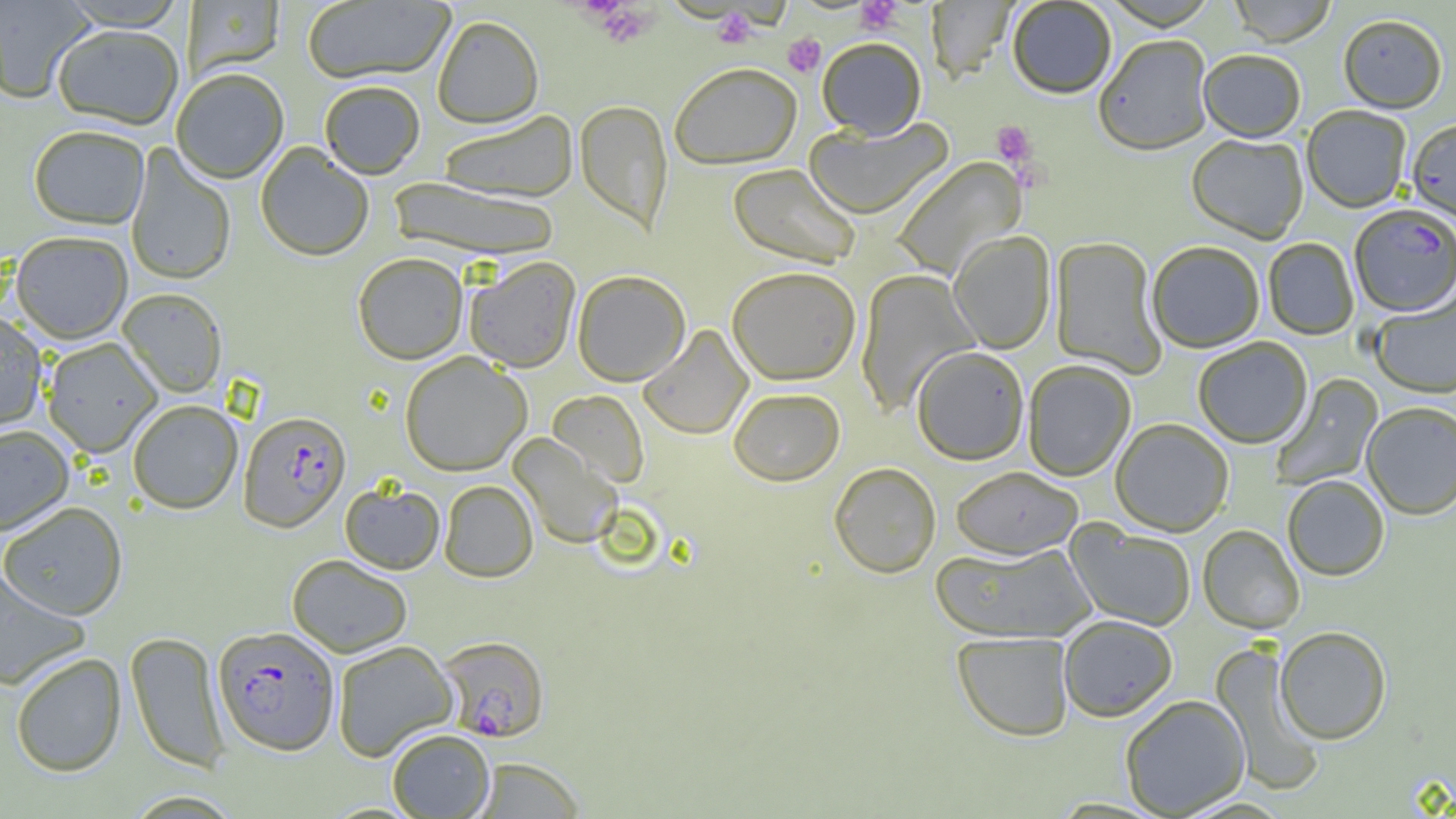

Summary:
  - Coordinate format: approximate bounding boxes as [x1, y1, x2, y2] in pixels
  - Uninfected red blood cell locations: [0, 0, 94, 105], [302, 0, 455, 86], [1102, 0, 1219, 32], [1228, 0, 1337, 48], [59, 1, 190, 32], [184, 1, 285, 80], [310, 1, 438, 178], [926, 1, 1017, 82], [1007, 1, 1116, 101], [433, 17, 544, 130], [1338, 17, 1447, 115], [53, 27, 183, 130], [1095, 38, 1213, 158], [817, 39, 926, 140], [1198, 52, 1305, 144], [670, 63, 802, 170], [171, 70, 288, 185], [319, 82, 425, 180], [575, 100, 673, 235], [1302, 108, 1411, 214], [437, 111, 579, 204], [804, 117, 954, 220], [1406, 120, 1456, 226], [28, 128, 149, 231], [1186, 136, 1308, 244], [125, 144, 236, 287], [255, 144, 374, 262], [891, 157, 1027, 281], [727, 163, 862, 270], [389, 178, 563, 263], [948, 231, 1056, 354], [11, 233, 132, 345], [1050, 237, 1167, 380], [1263, 238, 1358, 340], [1147, 242, 1265, 353], [353, 253, 468, 364], [464, 257, 581, 372], [727, 266, 861, 385], [855, 270, 981, 417], [572, 271, 691, 386], [117, 289, 227, 399], [1370, 291, 1456, 399], [0, 311, 47, 433], [638, 325, 753, 440], [1193, 338, 1313, 449], [42, 339, 162, 458], [912, 346, 1029, 465], [400, 352, 531, 476], [1023, 360, 1136, 481], [1270, 374, 1383, 491], [728, 387, 845, 486], [547, 390, 649, 488], [128, 401, 243, 515], [1362, 403, 1456, 520], [1111, 419, 1234, 537], [0, 426, 74, 535], [508, 433, 622, 549], [829, 462, 941, 578], [950, 466, 1083, 559], [1283, 476, 1389, 582], [439, 480, 538, 582], [340, 482, 445, 574], [0, 502, 127, 621], [1066, 523, 1196, 631], [1198, 525, 1304, 634], [929, 542, 1097, 644], [287, 554, 412, 657], [0, 569, 90, 689], [1059, 616, 1178, 723], [1276, 627, 1391, 745], [125, 631, 229, 774], [952, 632, 1074, 742], [332, 640, 457, 761], [1209, 641, 1327, 796], [11, 653, 126, 778], [1120, 695, 1250, 817], [387, 729, 495, 818], [471, 757, 585, 819], [123, 791, 244, 818]
  - Platelet locations: [855, 1, 903, 35], [592, 3, 656, 48], [712, 8, 759, 49], [783, 33, 826, 77], [990, 120, 1037, 166]
  - Plasmodium falciparum-infected red blood cell locations: [1349, 206, 1456, 318], [238, 412, 351, 532], [213, 626, 339, 756], [438, 635, 550, 742]
  - Slide-level diagnosis: Plasmodium falciparum
  - Modality: optical microscopy
  - Field of view: single
  - Image size: 1456×819 pixels
  - Magnification: 1000x
  - Preparation: thin blood film